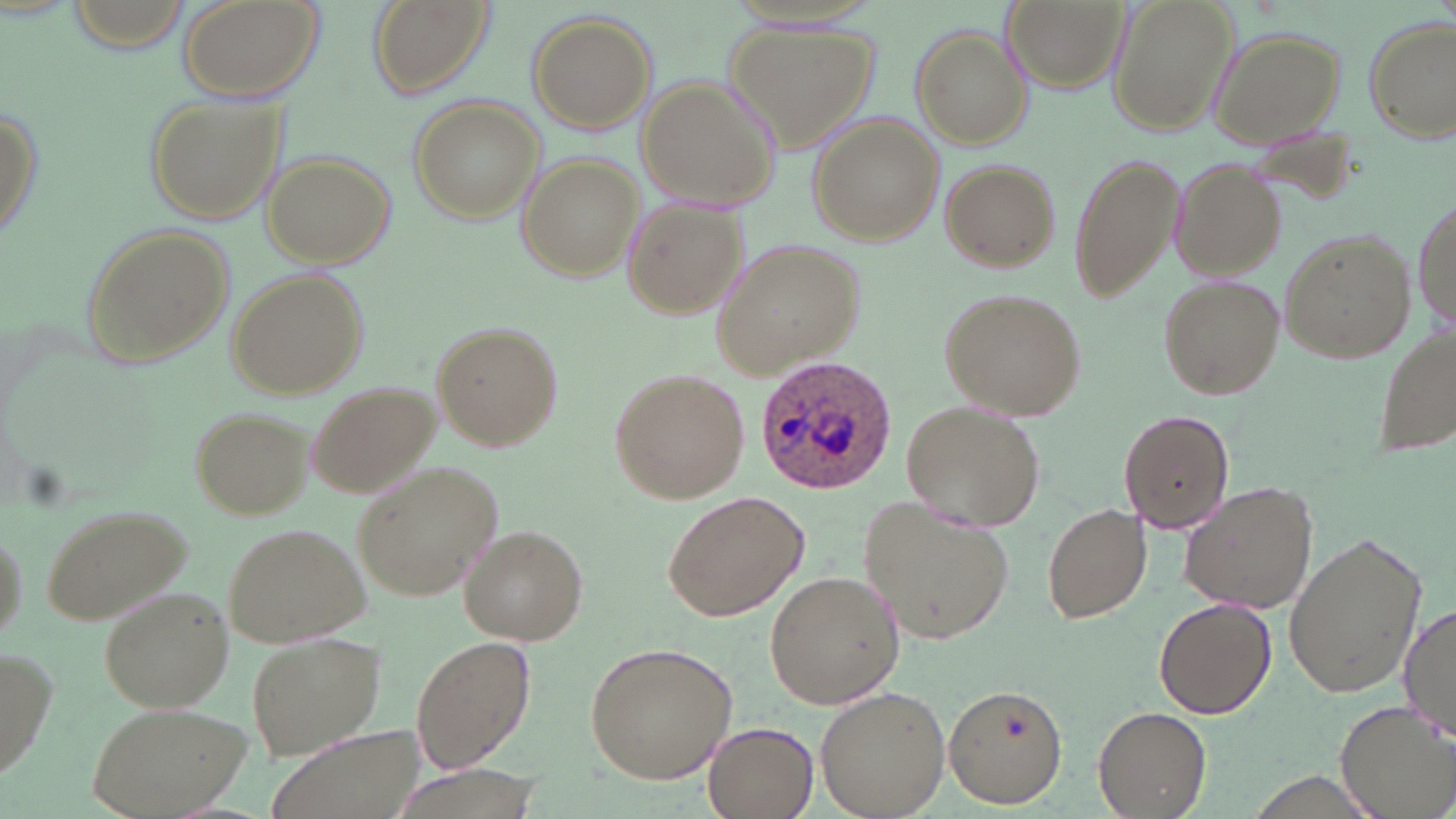
Summary:
  - Coordinate format: approximate bounding boxes as (x1,y1)-(x2,y2) corner pairs in pixels
  - Plasmodium ovale-infected red blood cell locations: (755,354)-(898,495)
  - Uninfected red blood cell locations: (177,0)-(323,103), (364,0)-(497,101), (1001,0)-(1130,96), (1105,0)-(1240,139), (526,10)-(657,135), (1364,16)-(1455,143), (729,19)-(878,154), (1207,25)-(1346,146), (910,27)-(1031,150), (637,76)-(779,211), (0,93)-(43,254), (144,94)-(283,224), (409,95)-(546,225), (810,114)-(943,244), (1067,149)-(1184,302), (261,152)-(396,266), (517,153)-(641,281), (1167,155)-(1285,282), (938,159)-(1059,271), (622,197)-(748,320), (1412,200)-(1454,337), (79,222)-(232,367), (1280,228)-(1418,366), (714,238)-(865,377), (226,270)-(369,400), (1158,275)-(1284,400), (939,287)-(1085,423), (1371,318)-(1456,463), (430,321)-(564,451), (610,366)-(750,504), (306,380)-(441,499), (903,401)-(1042,533), (187,405)-(311,520), (1119,409)-(1234,535), (354,465)-(496,598), (1177,481)-(1318,615), (661,491)-(809,624), (1042,500)-(1151,624), (860,501)-(1013,648), (41,502)-(194,625), (227,522)-(371,646), (460,527)-(586,644), (1282,530)-(1429,702), (764,569)-(905,709), (101,589)-(232,711), (1154,598)-(1275,718), (1401,602)-(1455,745), (248,629)-(386,758), (410,634)-(536,773), (584,641)-(738,783), (0,642)-(60,785), (944,684)-(1068,809), (815,685)-(953,818), (1335,698)-(1456,816), (88,700)-(250,818), (1093,704)-(1212,817), (704,722)-(818,818), (266,726)-(426,819)
  - Slide-level diagnosis: Plasmodium ovale
  - Image size: 1456×819 pixels
  - Stain: May-Grünwald-Giemsa
  - Field of view: single
  - Preparation: thin blood film
  - Modality: optical microscopy
  - Magnification: 1000x